Classify this cell by malaria status.
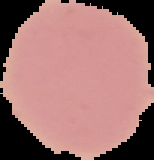

It is uninfected.

Image is 154×160 pixels. The area outside the segmented cell region is set to black. From a thin blood film.